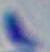
identification = Toxoplasma gondii
magnification = 1000x
modality = photomicrograph